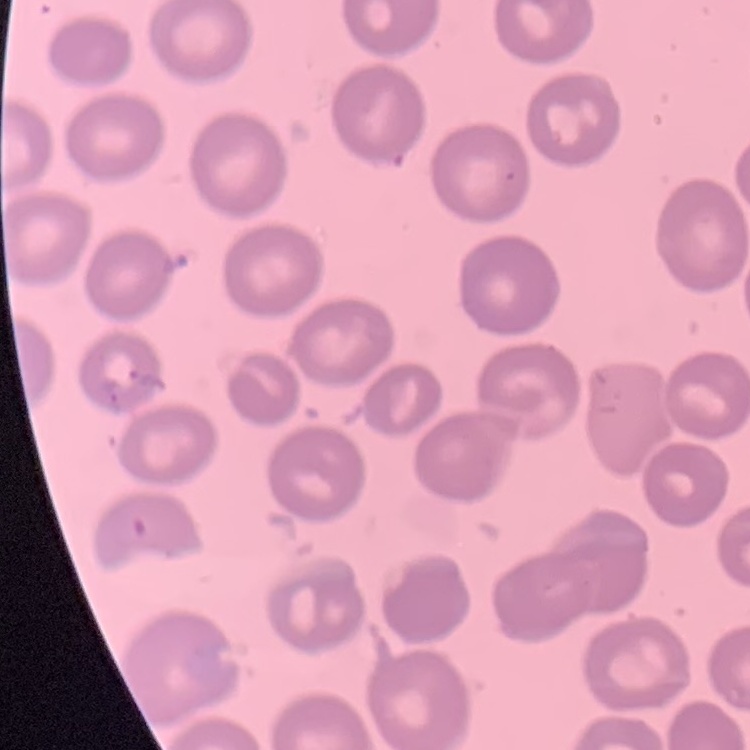
The erythrocytes show no rouleaux formation. Square crop of a larger photomicrograph. Field's or Giemsa stain. Thin blood film.